Report the malaria status of this cell.
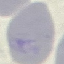
Uninfected.

Photographed with a smartphone camera at the microscope eyepiece. Automatically extracted cell patch, resized to 64 × 64 pixels. Thin blood film. Giemsa stain.